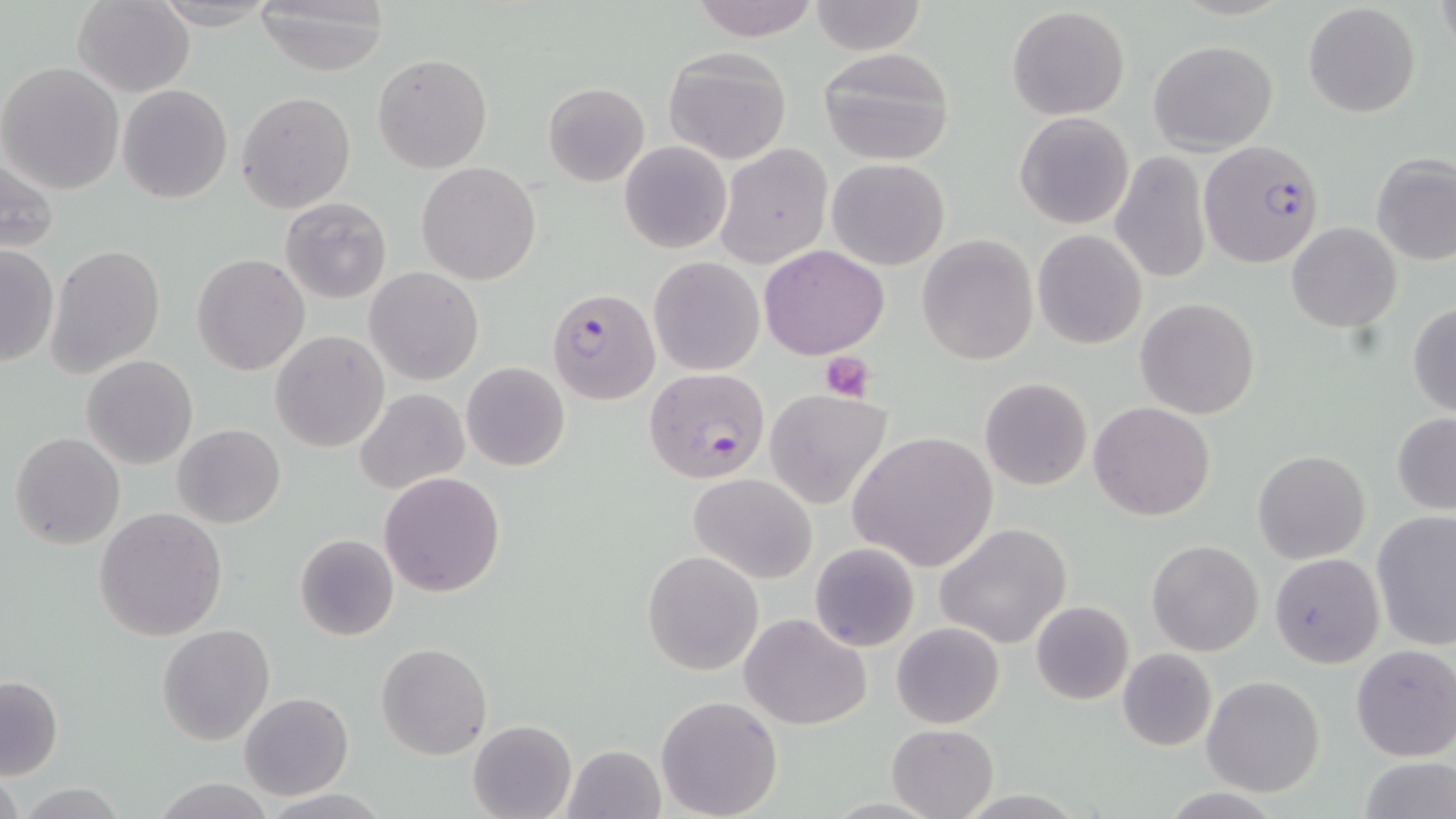

Summary:
  - Coordinate format: approximate bounding boxes as (x1, y1, x2, y2) in pixels
  - Plasmodium falciparum-infected red blood cell locations: (1197, 140, 1325, 270), (549, 288, 658, 404), (644, 368, 769, 483)
  - Uninfected red blood cell locations: (72, 0, 195, 97), (148, 0, 280, 28), (689, 0, 819, 40), (807, 1, 929, 54), (251, 2, 390, 74), (1303, 2, 1420, 118), (1006, 7, 1129, 119), (1149, 39, 1277, 153), (816, 46, 958, 167), (663, 48, 794, 165), (373, 53, 493, 173), (1, 62, 124, 194), (541, 81, 651, 187), (117, 84, 232, 204), (237, 91, 357, 212), (1014, 111, 1134, 230), (619, 139, 732, 254), (714, 145, 833, 269), (2, 150, 62, 257), (1110, 150, 1212, 284), (1371, 153, 1456, 268), (827, 158, 948, 270), (417, 163, 542, 284), (280, 197, 392, 303), (1287, 222, 1401, 332), (1032, 228, 1147, 350), (916, 234, 1038, 365), (46, 243, 165, 380), (0, 245, 60, 369), (759, 245, 889, 360), (192, 254, 310, 375), (648, 256, 763, 375), (365, 266, 484, 385), (1135, 297, 1260, 419), (1406, 301, 1456, 418), (270, 331, 390, 453), (82, 355, 198, 470), (461, 361, 569, 472), (978, 377, 1092, 492), (355, 388, 469, 494), (764, 388, 889, 510), (1089, 402, 1216, 520), (1391, 412, 1456, 516), (174, 423, 285, 528), (849, 430, 996, 572), (10, 432, 125, 549), (1252, 449, 1370, 564), (379, 472, 506, 596), (689, 472, 816, 583), (93, 508, 228, 640), (1371, 510, 1456, 650), (936, 523, 1073, 649), (294, 533, 400, 642), (1147, 538, 1263, 656), (810, 542, 919, 651), (641, 550, 763, 675), (1270, 553, 1384, 668), (1030, 600, 1134, 704), (740, 613, 874, 730), (891, 621, 1005, 730), (156, 623, 276, 746), (375, 642, 492, 760), (1351, 645, 1456, 762), (1117, 647, 1218, 751), (0, 674, 62, 781), (1201, 676, 1326, 796), (239, 692, 353, 801), (655, 695, 784, 819), (467, 719, 579, 819), (886, 722, 1000, 819), (560, 744, 665, 818), (1356, 757, 1453, 818), (1, 767, 23, 819), (152, 778, 276, 817), (17, 782, 130, 817)
  - Platelet locations: (818, 352, 876, 403)
  - Slide-level diagnosis: Plasmodium falciparum
  - Image size: 1456×819 pixels
  - Preparation: thin blood smear
  - Field of view: single
  - Modality: light microscopy
  - Stain: May-Grünwald-Giemsa
  - Magnification: 1000x